Assess this cell for malaria.
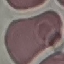
It is uninfected.

Photographed with a smartphone camera at the microscope eyepiece. Thin blood film. Cell patch, automatically extracted from a larger field of view and resized to 64 × 64 pixels. Giemsa stain.